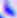

identification: Toxoplasma gondii
magnification: 400x
modality: micrograph